Point out each Plasmodium parasite.
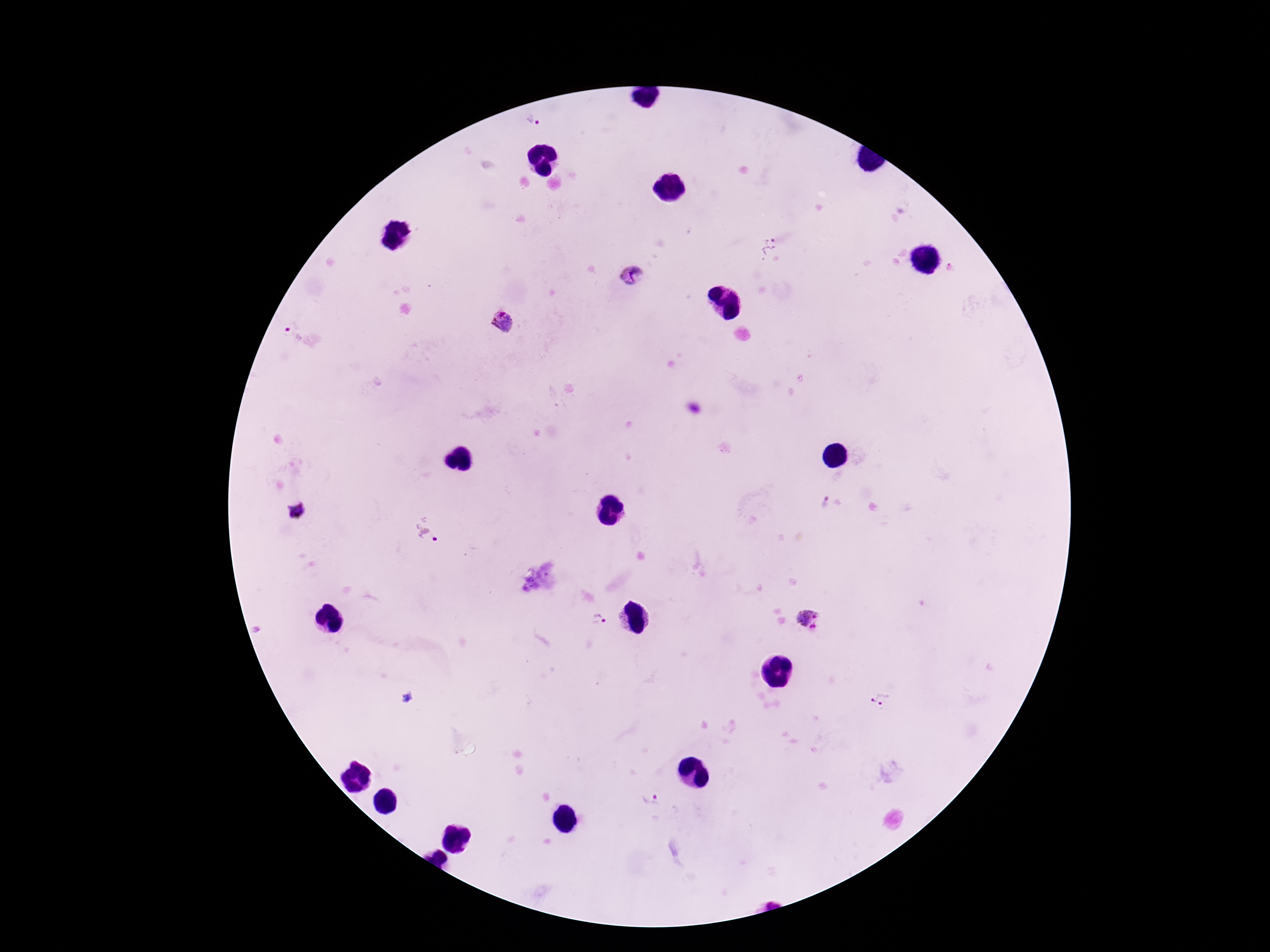

Approximate centers as (x, y) in pixels.
Plasmodium parasites: (534, 120), (773, 248), (632, 275), (504, 322), (291, 333), (826, 505), (295, 514), (425, 530), (813, 619), (602, 621), (880, 702), (653, 801).

stain = Giemsa
image size = 1270×952 pixels
patient malaria status = infected
field of view = one from this slide
preparation = thick peripheral-blood smear
capture = smartphone camera through the microscope eyepiece
magnification = 100x